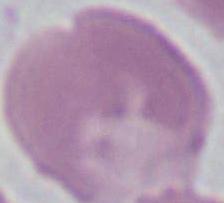 Captured at 1000x magnification. A red blood cell is shown. Photomicrograph.